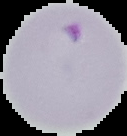
{
  "image_type": "segmented cell region on a black background",
  "result": "malaria parasites detected",
  "image_size": "127×136 pixels",
  "preparation": "thin blood film"
}